Outline each blood parasite and name the species.
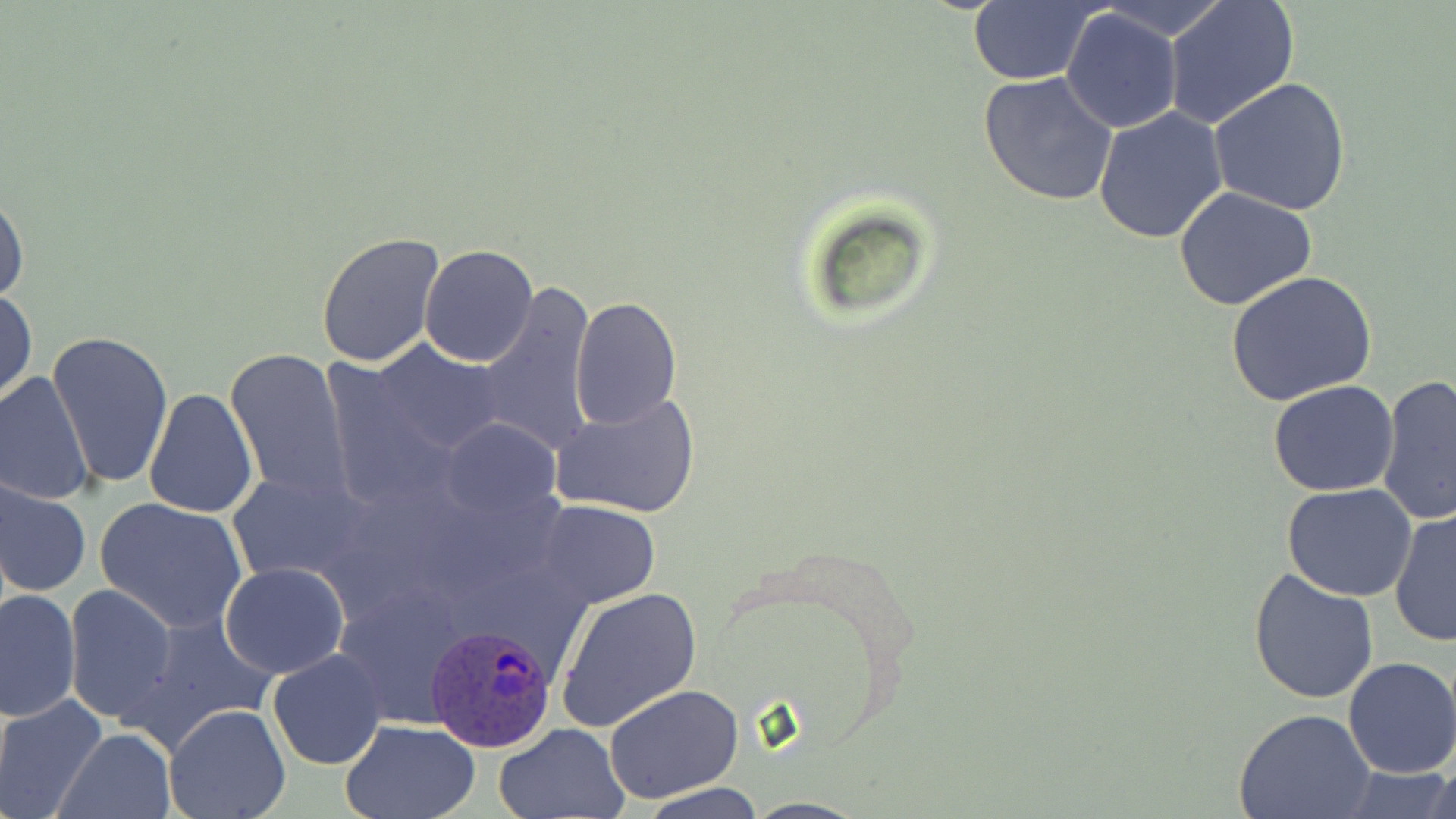
Approximate bounding boxes as [x1, y1, x2, y2] in pixels.
Plasmodium ovale-infected red blood cells: [427, 622, 559, 752].
No Plasmodium falciparum, Plasmodium malariae, Plasmodium vivax, Babesia divergens, or Trypanosoma brucei observed.

Uninfected red blood cell locations: [1096, 0, 1231, 41], [1164, 0, 1299, 129], [967, 3, 1098, 84], [1061, 7, 1183, 134], [977, 73, 1119, 209], [1208, 76, 1353, 217], [1093, 107, 1229, 246], [0, 187, 28, 310], [1173, 188, 1318, 314], [316, 231, 445, 367], [420, 245, 539, 366], [1226, 272, 1378, 408], [477, 280, 599, 456], [1, 289, 37, 406], [571, 296, 681, 431], [48, 329, 173, 490], [369, 341, 508, 455], [224, 346, 354, 501], [0, 371, 93, 507], [1376, 375, 1456, 527], [1268, 379, 1400, 496], [142, 386, 259, 519], [550, 392, 699, 521], [438, 419, 559, 524], [227, 471, 375, 585], [0, 478, 92, 598], [1283, 483, 1419, 601], [95, 497, 247, 634], [537, 500, 661, 607], [1389, 507, 1456, 649], [220, 562, 349, 679], [1247, 565, 1382, 705], [63, 584, 177, 727], [555, 586, 701, 733], [2, 588, 82, 722], [124, 611, 281, 750], [266, 648, 387, 770], [1342, 655, 1456, 779], [604, 684, 744, 802], [0, 694, 107, 818], [163, 703, 291, 819], [1233, 710, 1375, 819], [340, 718, 483, 818], [495, 723, 630, 819], [56, 728, 178, 819], [1427, 753, 1456, 818], [1338, 764, 1455, 819], [639, 785, 766, 818]. Slide-level diagnosis: Plasmodium ovale. Optical microscopy. Thin blood film. One field of a larger specimen. Image is 1456×819 pixels. Captured at 1000x magnification. May-Grünwald-Giemsa-stained preparation.